Comment on the morphology of the erythrocytes.
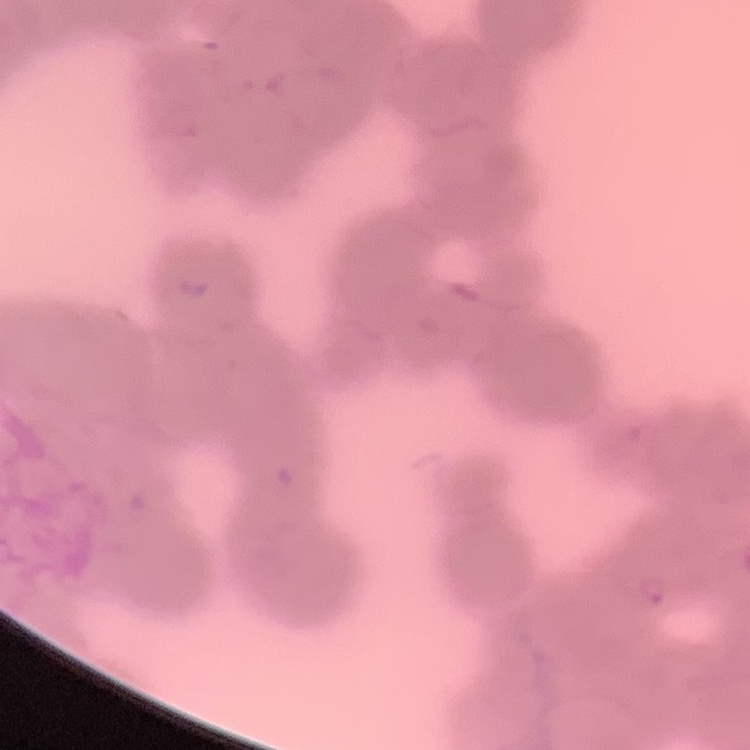
They show rouleaux formation.

Square crop of a larger photomicrograph. Stained with either Field's or Giemsa. Thin blood smear.